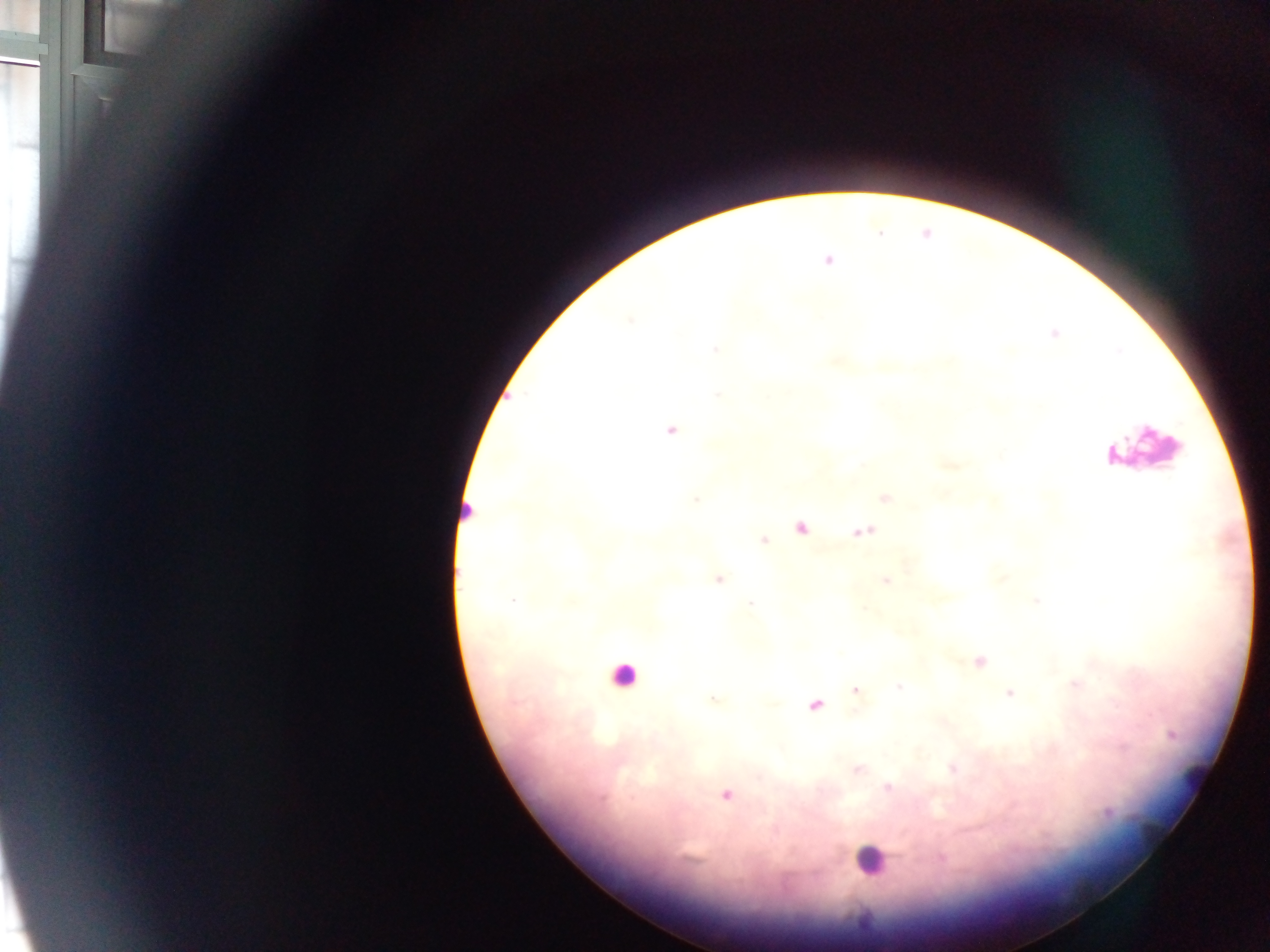
Approximate centers as (x, y) in pixels. Malaria parasite locations: (827, 261), (630, 320), (1054, 333), (715, 349), (717, 394), (672, 430), (885, 498), (696, 499), (801, 527), (863, 531), (764, 540), (718, 579), (885, 581), (513, 601), (1037, 601), (751, 604), (980, 661), (1075, 684), (899, 686), (855, 690), (1010, 694), (712, 699), (815, 706), (1171, 734), (1123, 747), (857, 769), (952, 769), (888, 788), (726, 796), (1108, 813), (941, 858). Leukocyte locations: (1144, 449), (463, 513), (623, 675), (870, 859). Photographed through a microscope with a mobile-phone camera. Sample from Ghana. Single field of view. Image is 1270×952 pixels. Thick blood film.